Outline each blood parasite and name the species.
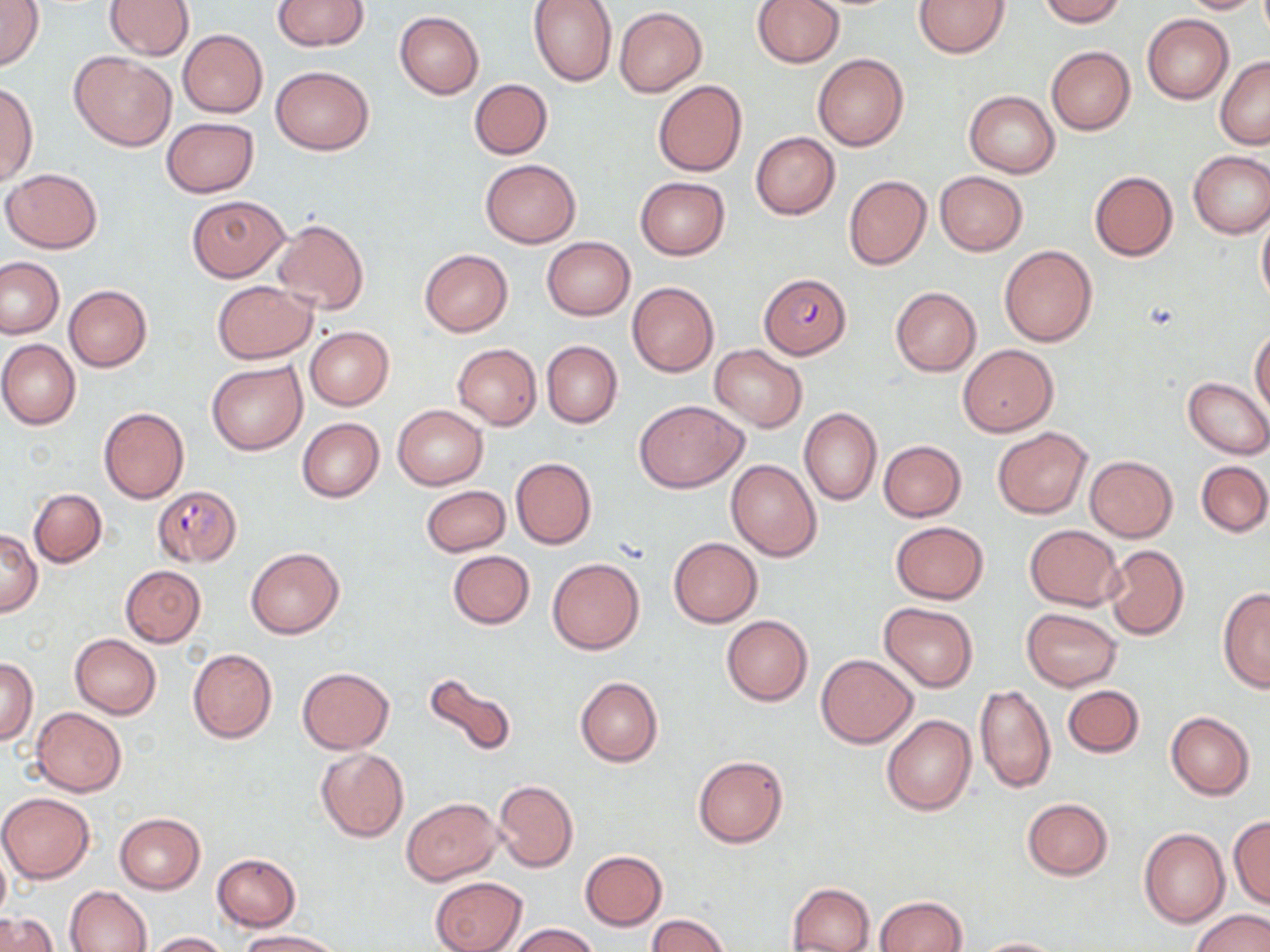
Approximate bounding boxes as (x1,y1)-(x2,y2) corner pairs in pixels.
Plasmodium falciparum-infected red blood cells: (760,273)-(850,358), (151,484)-(242,565).
No Plasmodium ovale, Plasmodium malariae, Plasmodium vivax, Babesia divergens, or Trypanosoma brucei observed.

Uninfected red blood cell locations: (0,0)-(45,73), (272,0)-(368,50), (529,0)-(618,86), (914,0)-(1011,57), (1038,0)-(1126,26), (1177,0)-(1264,14), (104,1)-(194,60), (752,1)-(843,68), (614,7)-(708,96), (394,11)-(484,98), (1142,14)-(1233,104), (179,30)-(268,118), (1046,46)-(1135,134), (70,50)-(176,150), (813,52)-(909,151), (1215,55)-(1270,149), (269,65)-(374,154), (469,79)-(552,159), (653,80)-(746,176), (0,84)-(37,185), (964,90)-(1060,177), (161,117)-(259,197), (751,132)-(839,219), (1188,151)-(1270,237), (480,159)-(581,247), (1,168)-(102,254), (934,171)-(1027,256), (1088,171)-(1178,261), (843,176)-(932,270), (635,177)-(730,260), (188,195)-(289,281), (1256,209)-(1270,309), (273,218)-(369,315), (542,237)-(635,320), (999,245)-(1096,347), (419,249)-(513,336), (1,256)-(65,339), (211,279)-(316,363), (627,281)-(718,376), (64,285)-(151,372), (890,287)-(981,375), (305,327)-(394,410), (1250,328)-(1270,415), (0,339)-(81,429), (541,340)-(622,428), (452,343)-(541,429), (709,344)-(808,432), (959,344)-(1058,437), (207,361)-(307,455), (1183,376)-(1270,457), (635,400)-(748,492), (392,405)-(488,490), (98,407)-(190,504), (798,407)-(881,505), (296,418)-(384,502), (992,427)-(1092,518), (879,440)-(966,521), (1085,456)-(1177,541), (511,457)-(596,548), (1196,459)-(1269,537), (727,460)-(821,560), (421,486)-(511,556), (29,488)-(106,567), (890,522)-(990,604), (1025,525)-(1123,611), (0,528)-(42,617), (669,537)-(763,628), (1105,545)-(1189,640), (246,547)-(344,638), (447,550)-(536,629), (548,557)-(645,655), (120,565)-(204,647), (1218,588)-(1270,690), (878,601)-(979,691), (1021,608)-(1122,691), (721,615)-(812,706), (69,633)-(161,718), (187,649)-(277,742), (815,654)-(918,748), (1,658)-(39,743), (296,667)-(395,753), (423,669)-(517,762), (575,676)-(663,767), (1061,684)-(1144,758), (974,685)-(1056,793), (30,706)-(126,796), (1166,712)-(1255,800), (881,715)-(976,817), (315,748)-(408,842), (692,753)-(789,849), (494,781)-(579,873), (1,792)-(95,883), (401,796)-(502,885), (1022,797)-(1112,880), (115,813)-(206,893), (1228,815)-(1270,908), (1138,829)-(1229,927), (0,844)-(10,928), (580,850)-(667,929), (212,854)-(301,931), (430,876)-(526,952), (788,882)-(874,952), (65,886)-(152,952), (876,895)-(967,951), (1191,909)-(1269,952), (3,913)-(58,951), (646,913)-(731,951), (507,923)-(600,952), (237,930)-(345,951), (144,931)-(230,951), (970,936)-(1065,952). Slide-level diagnosis: Plasmodium falciparum. May-Grünwald-Giemsa-stained preparation. Thin blood film. Light microscopy. 1000x magnification. Image is 1270×952 pixels. Single field of view.